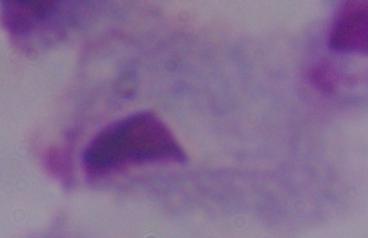 A trichomonad is shown. 1000x magnification. Micrograph.